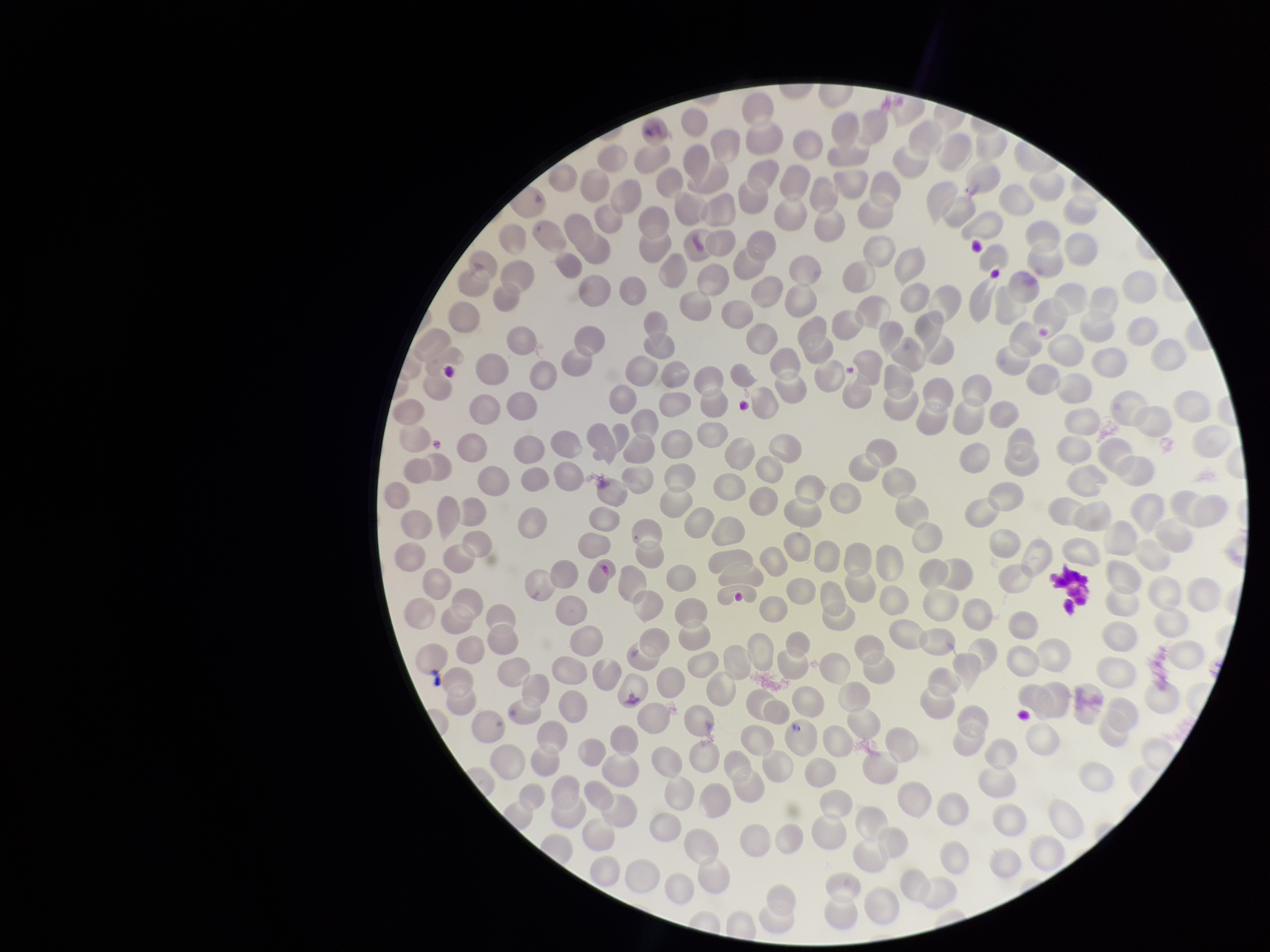
Patient malaria status: infected. Smartphone photograph taken through the eyepiece of a microscope. Stained with Giemsa. Single field of view. Red blood cell count: 229. Image is 1270×952 pixels. Parasitized red blood cells: none seen. Species reported for this patient: Plasmodium vivax. Parasitized red blood cell count: 0. Preparation: thin blood smear.